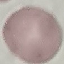
malaria status = uninfected
preparation = thin smear
image type = cell patch, automatically extracted from a larger field of view and resized to 64 × 64 pixels
capture = smartphone camera at the microscope eyepiece
stain = Giemsa